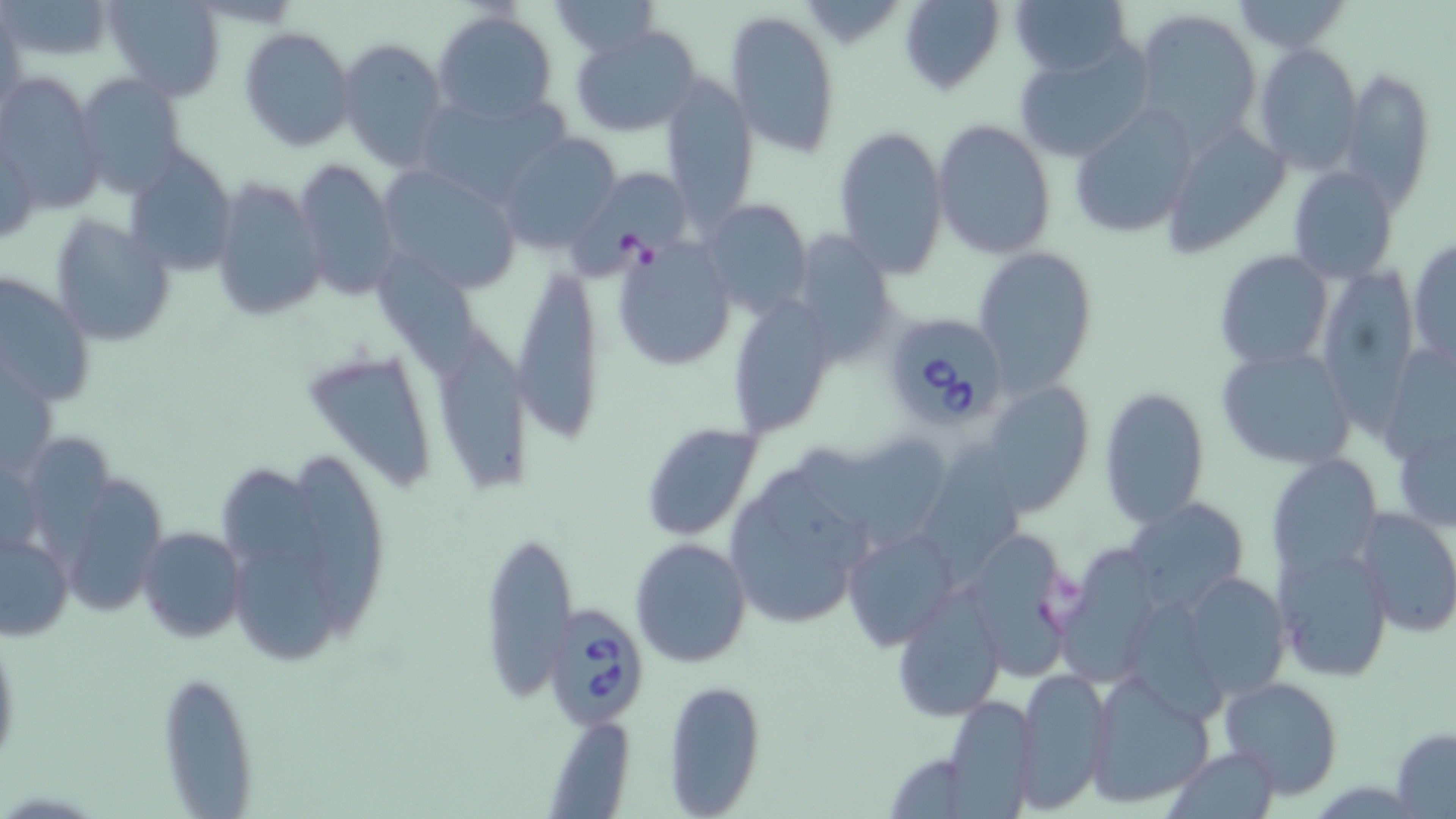

Approximate bounding boxes as [x1, y1, x2, y2] in pixels. Uninfected red blood cell locations: [3, 0, 116, 60], [104, 0, 226, 101], [548, 0, 660, 58], [898, 0, 1006, 95], [1010, 0, 1133, 76], [1227, 0, 1355, 54], [1131, 7, 1264, 142], [725, 9, 842, 159], [433, 10, 558, 124], [1, 15, 26, 119], [569, 25, 702, 137], [238, 26, 355, 152], [336, 37, 448, 169], [1011, 42, 1153, 164], [1252, 42, 1364, 174], [1341, 67, 1435, 208], [0, 73, 104, 208], [77, 74, 187, 195], [658, 76, 759, 223], [411, 91, 573, 208], [1067, 106, 1201, 238], [932, 119, 1057, 258], [1166, 121, 1292, 257], [832, 126, 947, 277], [496, 131, 624, 255], [123, 148, 238, 275], [295, 159, 399, 302], [569, 162, 693, 285], [378, 164, 523, 295], [1288, 165, 1399, 284], [210, 176, 328, 322], [698, 197, 814, 315], [49, 213, 177, 348], [789, 231, 898, 363], [613, 238, 737, 371], [1407, 238, 1456, 369], [974, 246, 1099, 395], [1212, 250, 1334, 369], [375, 256, 484, 394], [510, 263, 606, 450], [1317, 263, 1417, 439], [0, 273, 92, 410], [726, 294, 840, 441], [443, 335, 536, 500], [1215, 344, 1358, 470], [306, 347, 445, 492], [979, 380, 1097, 517], [1098, 388, 1210, 526], [1390, 412, 1456, 536], [645, 418, 767, 538], [35, 437, 126, 574], [925, 440, 1023, 589], [799, 441, 946, 543], [1267, 453, 1382, 580], [296, 460, 388, 652], [68, 472, 172, 622], [216, 474, 329, 579], [1125, 497, 1250, 615], [728, 502, 849, 630], [1356, 505, 1456, 638], [136, 526, 246, 642], [841, 526, 958, 652], [479, 527, 577, 707], [957, 528, 1072, 679], [1, 530, 74, 641], [629, 537, 751, 668], [1052, 538, 1171, 686], [1273, 538, 1395, 681], [236, 553, 340, 662], [1176, 571, 1290, 699], [894, 587, 1006, 722], [1129, 599, 1232, 723], [1014, 668, 1112, 811], [155, 670, 259, 816], [1086, 673, 1214, 808], [1219, 676, 1345, 799], [662, 680, 767, 816], [942, 695, 1039, 817], [540, 712, 639, 817], [1390, 728, 1456, 818], [1165, 746, 1280, 819]. Babesia divergens-infected red blood cell locations: [879, 311, 1010, 432], [549, 604, 644, 730]. Slide-level diagnosis: Babesia divergens. 1000x magnification. Image is 1456×819 pixels. Thin blood film. Optical microscopy. May-Grünwald-Giemsa stain. One field of a larger specimen.